Identify the blood parasite species.
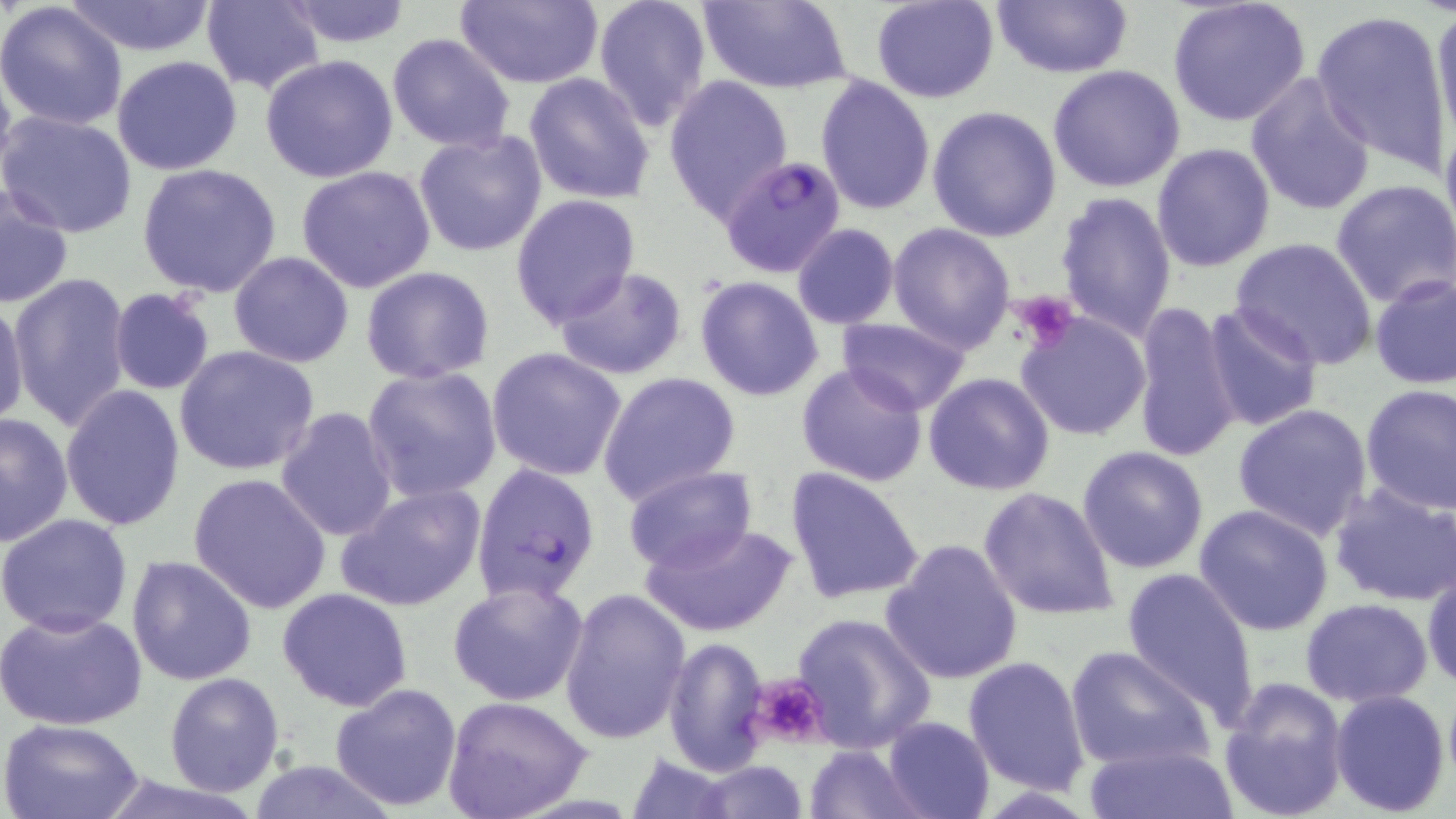

Plasmodium falciparum.

stain = May-Grünwald-Giemsa
modality = light microscopy
preparation = thin blood smear
magnification = 1000x
Plasmodium falciparum-infected red blood cell locations = approximate bounding boxes as (x1,y1)-(x2,y2) corner pairs in pixels: (718,154)-(848,277), (469,462)-(600,605)
uninfected red blood cell locations = approximate bounding boxes as (x1,y1)-(x2,y2) corner pairs in pixels: (280,0)-(412,48), (592,0)-(713,132), (697,0)-(851,91), (871,0)-(999,103), (990,0)-(1133,78), (1167,0)-(1312,127), (61,1)-(218,56), (202,1)-(327,94), (453,1)-(604,88), (0,3)-(129,133), (1431,6)-(1456,155), (1311,9)-(1455,171), (387,33)-(515,152), (112,54)-(242,175), (260,55)-(399,183), (1048,64)-(1185,192), (1245,72)-(1377,215), (524,73)-(656,207), (662,74)-(793,220), (815,75)-(936,215), (928,104)-(1062,242), (1437,110)-(1456,255), (1,111)-(138,238), (414,130)-(548,258), (1152,142)-(1276,271), (137,164)-(283,300), (296,165)-(437,292), (1331,177)-(1456,309), (1,183)-(74,309), (1054,190)-(1177,341), (510,193)-(640,329), (888,223)-(1015,352), (790,224)-(899,329), (1228,237)-(1379,373), (228,252)-(355,367), (361,266)-(495,384), (556,267)-(688,380), (8,271)-(133,432), (1369,273)-(1455,388), (694,276)-(824,402), (108,289)-(216,395), (0,297)-(28,432), (1132,301)-(1241,464), (1203,302)-(1323,431), (1013,310)-(1153,442), (836,316)-(971,417), (173,345)-(321,476), (486,347)-(629,482), (795,361)-(928,486), (362,366)-(502,503), (597,371)-(740,508), (923,372)-(1054,495), (59,384)-(186,530), (1359,384)-(1456,515), (1231,402)-(1374,542), (275,406)-(399,543), (0,412)-(73,545), (1076,445)-(1209,573), (623,466)-(757,573), (785,466)-(926,605), (187,472)-(333,614), (1330,481)-(1456,607), (336,482)-(485,613), (977,485)-(1120,621), (1193,503)-(1333,635), (0,513)-(133,637), (643,520)-(795,638), (880,538)-(1024,684), (128,554)-(258,685), (1422,564)-(1456,693), (1122,566)-(1261,727), (447,578)-(589,705), (277,587)-(413,711), (559,587)-(693,746), (1301,597)-(1432,706), (0,607)-(149,731), (790,612)-(937,754), (662,637)-(770,775), (1064,644)-(1214,773), (964,655)-(1092,796), (164,671)-(285,795), (1218,678)-(1349,819), (329,683)-(462,811), (1330,688)-(1451,814), (443,696)-(593,819), (882,716)-(994,819), (0,718)-(148,819), (1082,742)-(1239,818), (802,743)-(925,818), (621,751)-(737,817), (689,758)-(811,819), (243,759)-(401,817)
image size = 1456×819 pixels
field of view = single
platelet locations = approximate bounding boxes as (x1,y1)-(x2,y2) corner pairs in pixels: (1009,291)-(1079,352), (748,675)-(833,747)